Classify this cell by malaria status.
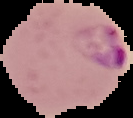

Parasitized.

Summary:
  - Image size: 133×118 pixels
  - Preparation: thin blood smear
  - Image type: segmented cell region with the area outside set to black